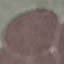
Summary:
  - Malaria status: uninfected
  - Preparation: thin blood smear
  - Image type: cell patch, automatically extracted from a larger field of view and resized to 64 × 64 pixels
  - Capture: smartphone camera at the microscope eyepiece
  - Stain: Giemsa